State which parasite is depicted.
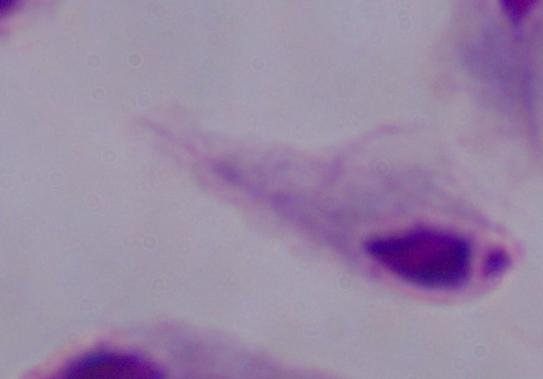

This is a trichomonad.

Micrograph. 1000x magnification.